Report the malaria status of this cell.
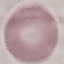
Uninfected.

image type = automatically extracted cell patch, resized to 64 × 64 pixels
capture = smartphone camera at the microscope eyepiece
stain = Giemsa
preparation = thin smear